State which parasite is depicted.
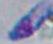

Toxoplasma gondii.

magnification = 1000x
modality = photomicrograph